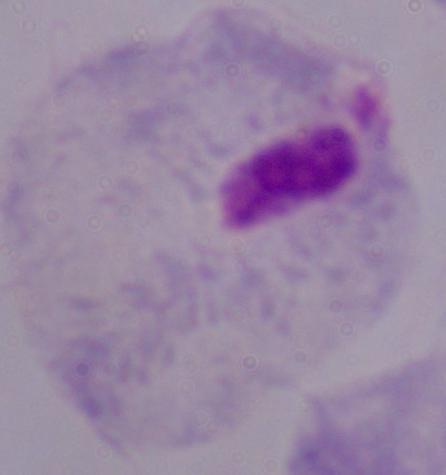
Summary:
  - Magnification: 1000x
  - Modality: photomicrograph
  - Identification: trichomonad